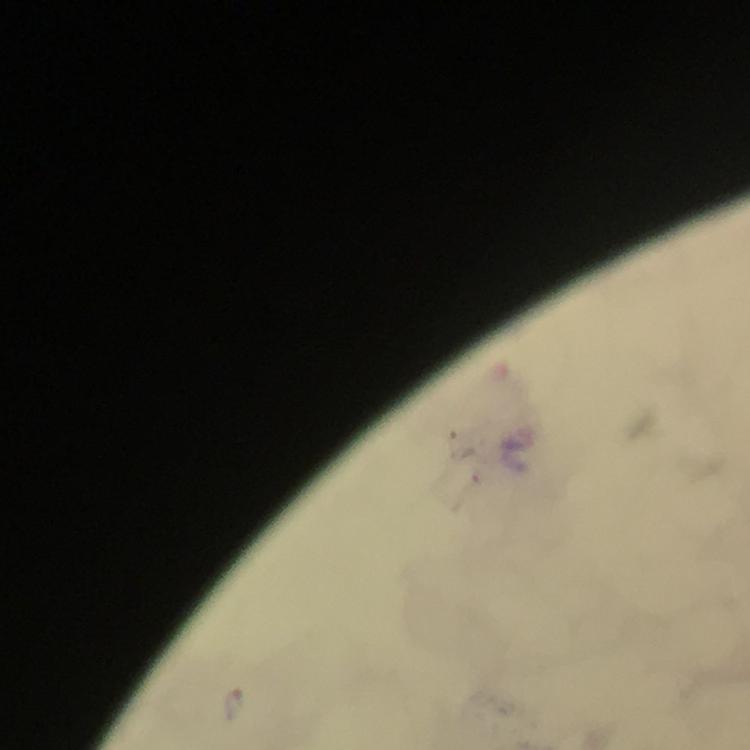
Approximate object centers, in pixels from the top-left corner.
Summary:
  - Malaria parasite locations: (x=236, y=706)
  - Magnification: 100x
  - Immersion oil: applied
  - Preparation: thick blood smear
  - Stain: Giemsa
  - Cropped from: one field of view
  - Capture: smartphone mounted on the microscope
  - Image size: 750×750 pixels
  - Context: from a malaria diagnostic workup